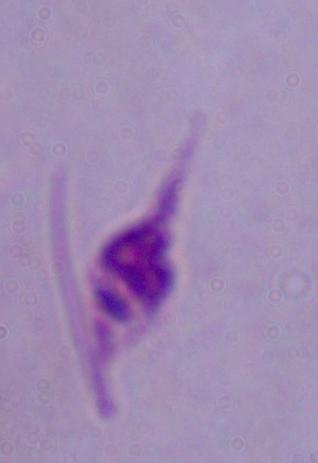 A Leishmania parasite is shown. Photomicrograph. Captured at 1000x magnification.